Classify this cell by malaria status.
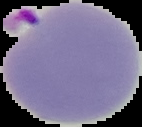
Parasitized.

Summary:
  - Image type: cell region segmented out of the field of view; surrounding area masked to black
  - Image size: 142×127 pixels
  - Preparation: thin blood smear